State which parasite is depicted.
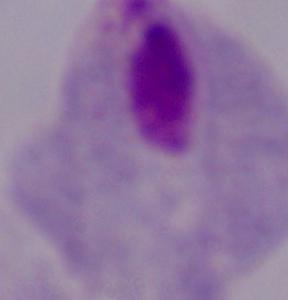

A trichomonad.

{
  "modality": "photomicrograph",
  "magnification": "1000x"
}